Comment on the morphology of the red blood cells.
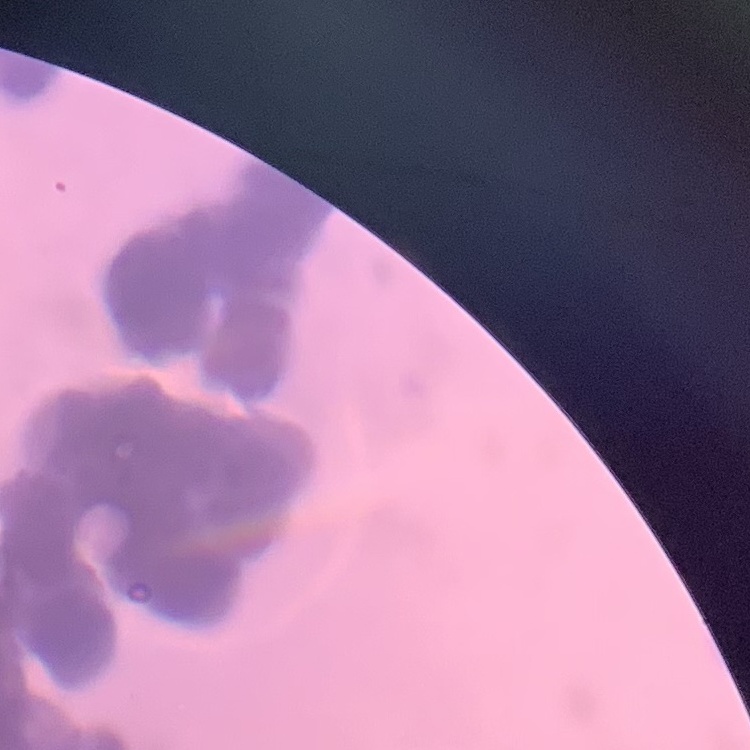
They show rouleaux formation.

Summary:
  - Stain: Field's or Giemsa
  - Preparation: thin peripheral smear
  - Image type: one tile cut from a larger photomicrograph